Identify the parasite.
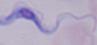

A trypanosome.

Summary:
  - Modality: micrograph
  - Magnification: 1000x